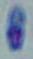
Photomicrograph. Captured at 1000x magnification. Toxoplasma gondii is shown.